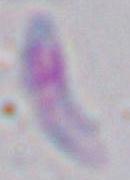
Summary:
  - Identification: Toxoplasma gondii
  - Modality: micrograph
  - Magnification: 1000x